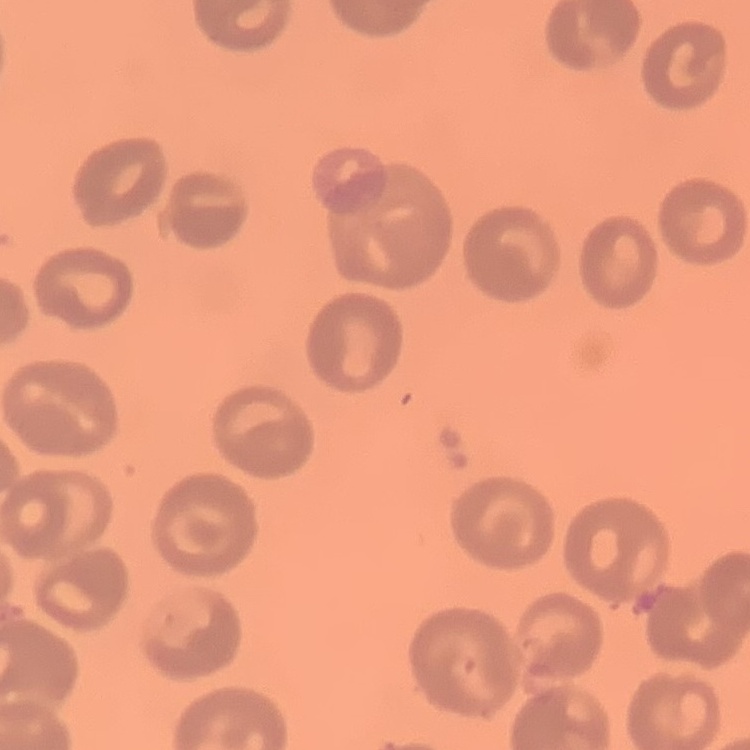

erythrocyte morphology = no rouleaux formation
preparation = thin blood smear
stain = Field's or Giemsa
image type = square crop of a larger photomicrograph